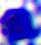

identification = leukocyte
magnification = 400x
modality = photomicrograph